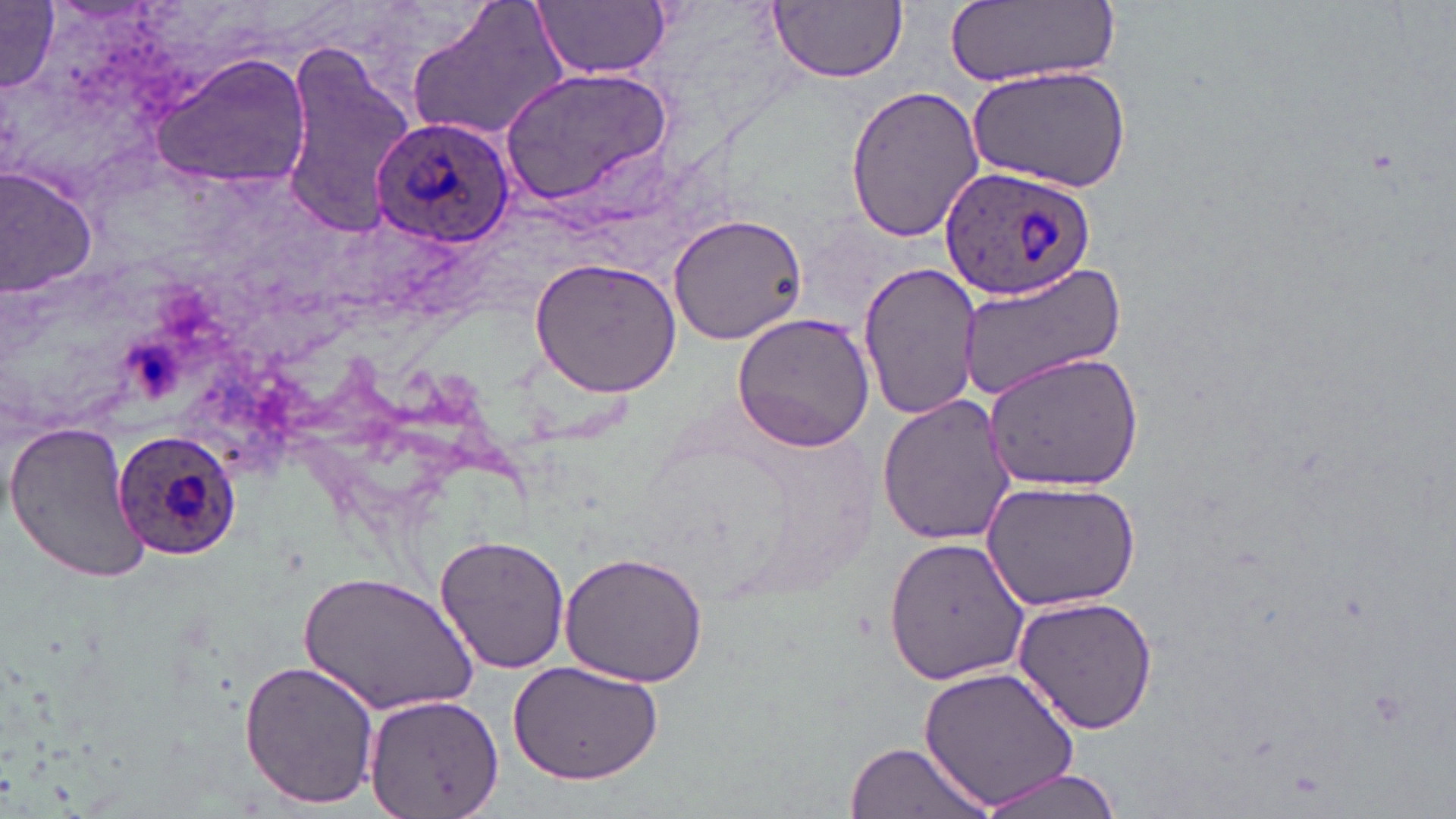 Approximate bounding boxes as (x1, y1, x2, y2) in pixels. Plasmodium ovale-infected red blood cell locations: (370, 115, 516, 247), (940, 166, 1097, 301), (107, 425, 240, 562). Uninfected red blood cell locations: (408, 0, 568, 142), (535, 0, 671, 79), (944, 0, 1117, 87), (767, 1, 906, 83), (0, 3, 60, 96), (280, 47, 413, 232), (152, 56, 313, 194), (967, 63, 1133, 194), (497, 64, 675, 207), (845, 82, 985, 242), (0, 165, 100, 298), (666, 211, 808, 345), (529, 257, 683, 398), (857, 260, 983, 421), (955, 261, 1127, 402), (730, 313, 877, 451), (982, 350, 1143, 493), (876, 392, 1020, 548), (5, 419, 152, 585), (979, 478, 1142, 614), (434, 532, 570, 674), (882, 534, 1032, 688), (557, 550, 710, 688), (301, 571, 476, 717), (1014, 594, 1158, 735), (239, 659, 381, 810), (507, 659, 666, 786), (916, 665, 1080, 807), (363, 694, 502, 819), (843, 739, 992, 819), (975, 768, 1123, 819). Slide-level diagnosis: Plasmodium ovale. Image is 1456×819 pixels. 1000x magnification. Optical microscopy. One field of a larger specimen. Thin blood smear. May-Grünwald-Giemsa stain.